Comment on the morphology of the erythrocytes.
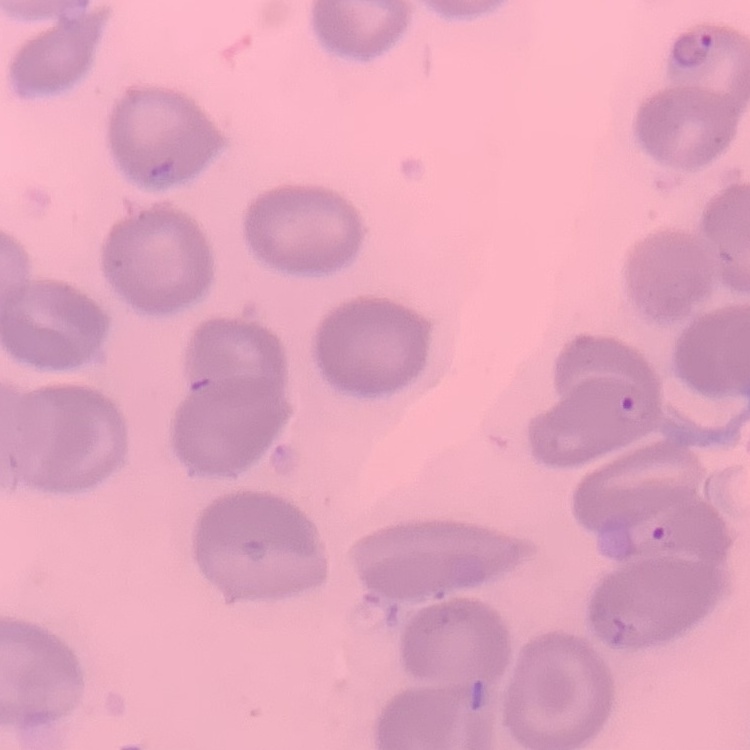
They show no rouleaux formation.

stain = Field's or Giemsa
image type = square crop of a larger photomicrograph
preparation = thin blood smear